Assess this cell for malaria.
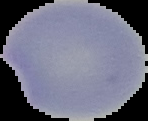

It is uninfected.

Summary:
  - Image type: cell region segmented out of the field of view; surrounding area masked to black
  - Image size: 148×121 pixels
  - Preparation: thin blood film